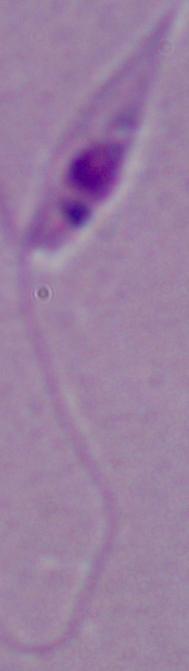

Summary:
  - Magnification: 1000x
  - Modality: micrograph
  - Identification: Leishmania